Assess for malaria.
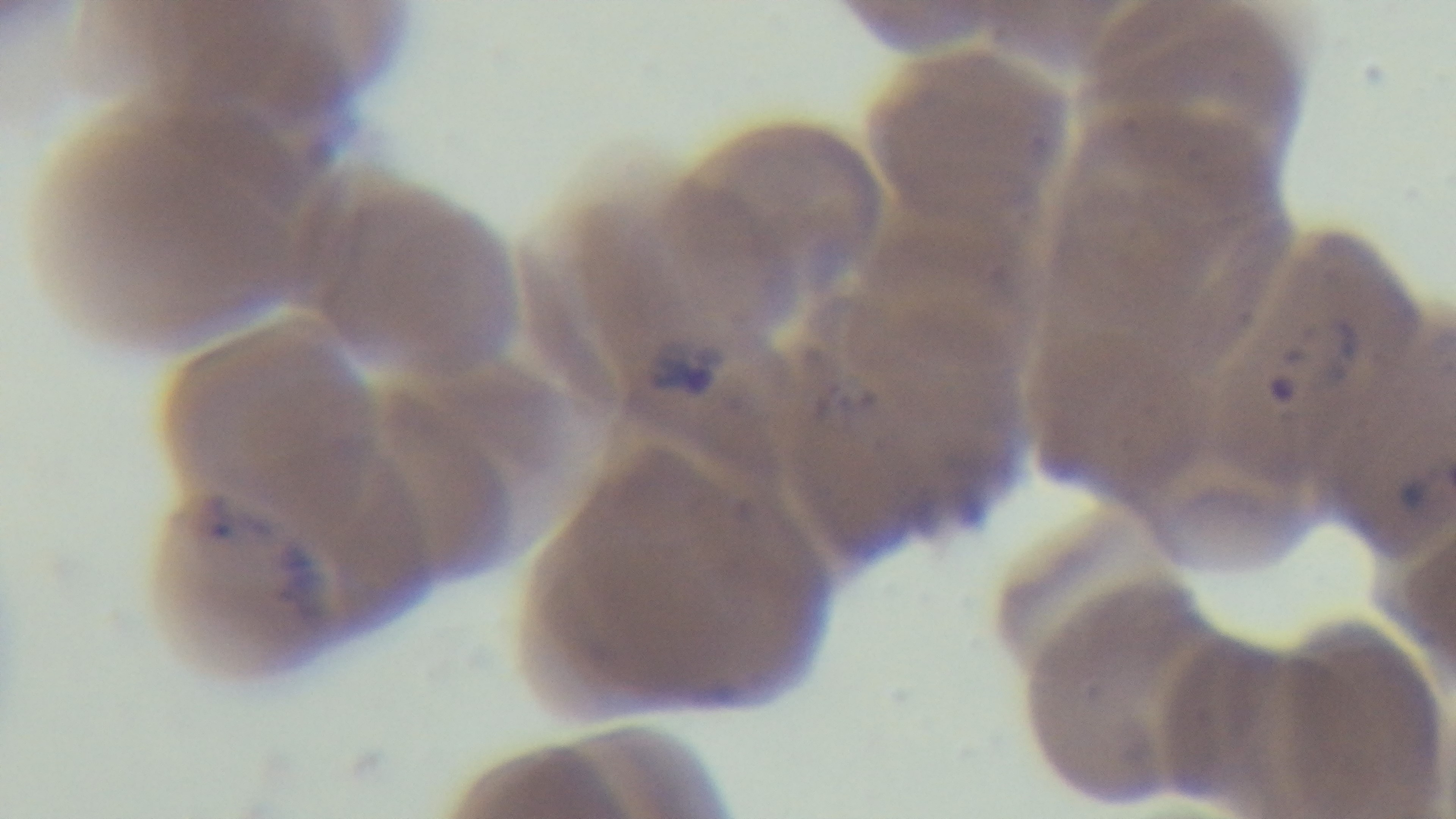
Infected.

100x oil-immersion objective. Giemsa-stained. Preparation: thin blood film. Captured with a mounted 4K digital camera. Photomicrograph. One field from the slide.